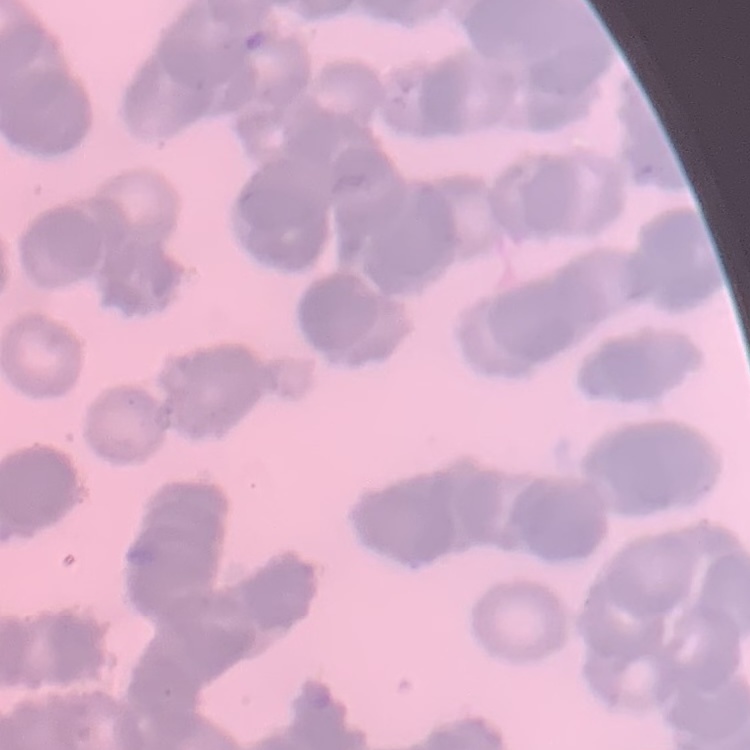

The erythrocytes exhibit rouleaux formation. Square crop of a larger photomicrograph. Thin peripheral smear. Field's or Giemsa stain.